Name the parasite shown.
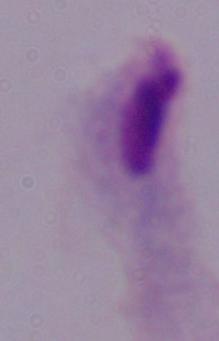

This is a trichomonad.

1000x magnification. Photomicrograph.